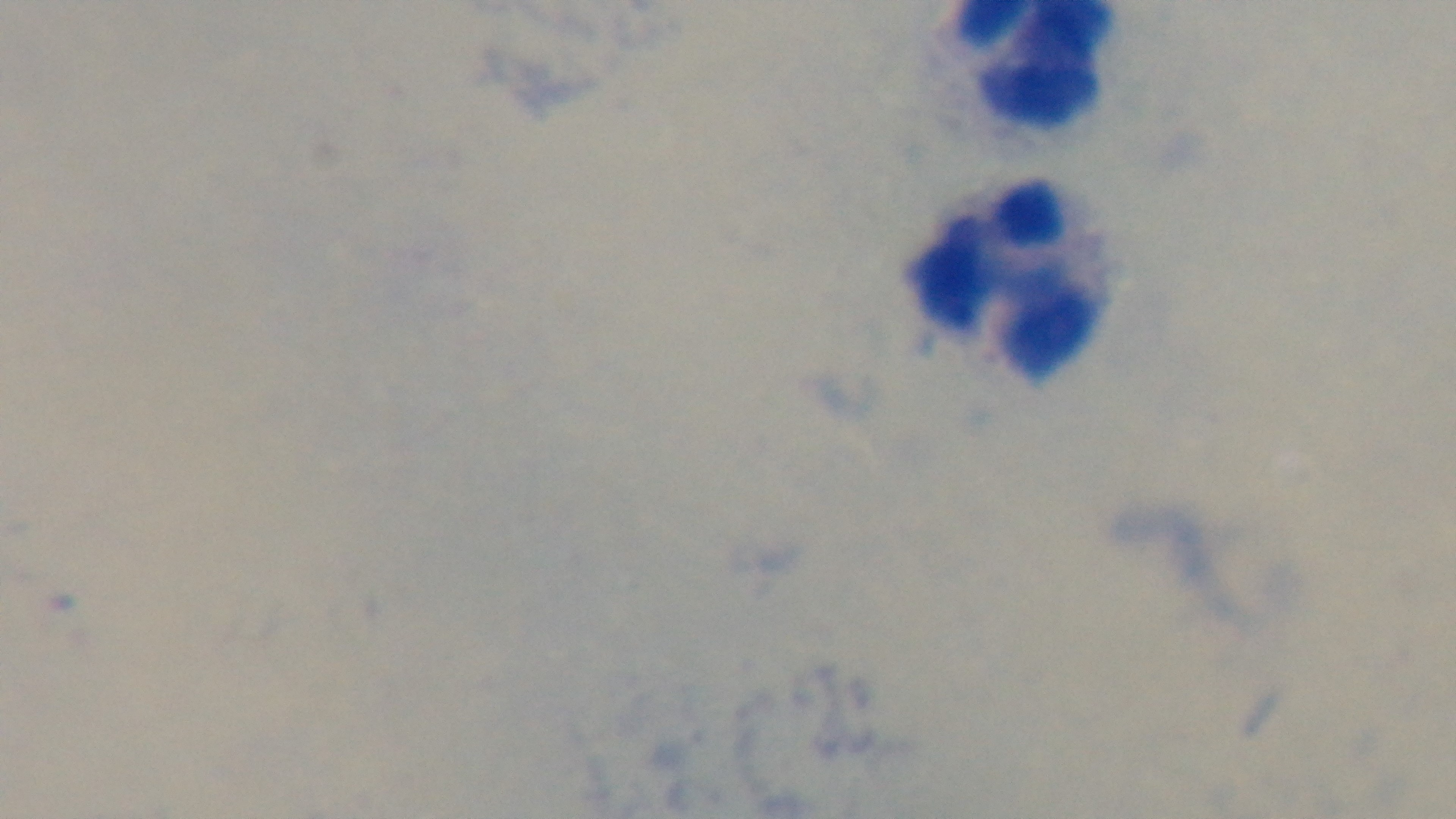
Summary:
  - Field of view: one from the slide
  - Stain: Giemsa
  - Capture: mounted 4K digital camera
  - Preparation: thick
  - Objective: 100x oil immersion
  - Modality: light microscopy
  - Malaria status: negative